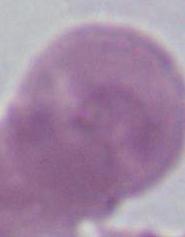

1000x magnification. Photomicrograph. An erythrocyte is seen.